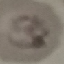
result = malaria parasites identified
preparation = thin blood smear
image type = automatically extracted cell patch, resized to 64 × 64 pixels
capture = smartphone through the microscope eyepiece
stain = Giemsa